Report the malaria status of this cell.
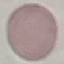
Uninfected.

Summary:
  - Stain: Giemsa
  - Preparation: thin blood smear
  - Capture: smartphone camera at the microscope eyepiece
  - Image type: automatically extracted cell patch, resized to 64 × 64 pixels